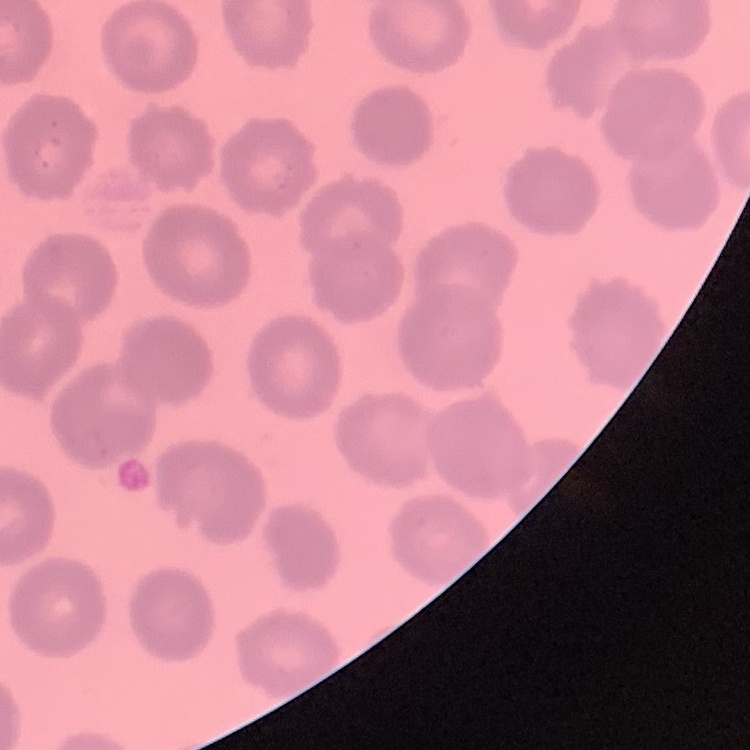
red blood cell morphology = no rouleaux formation
preparation = thin peripheral smear
image type = square crop of a larger photomicrograph
stain = Field's or Giemsa